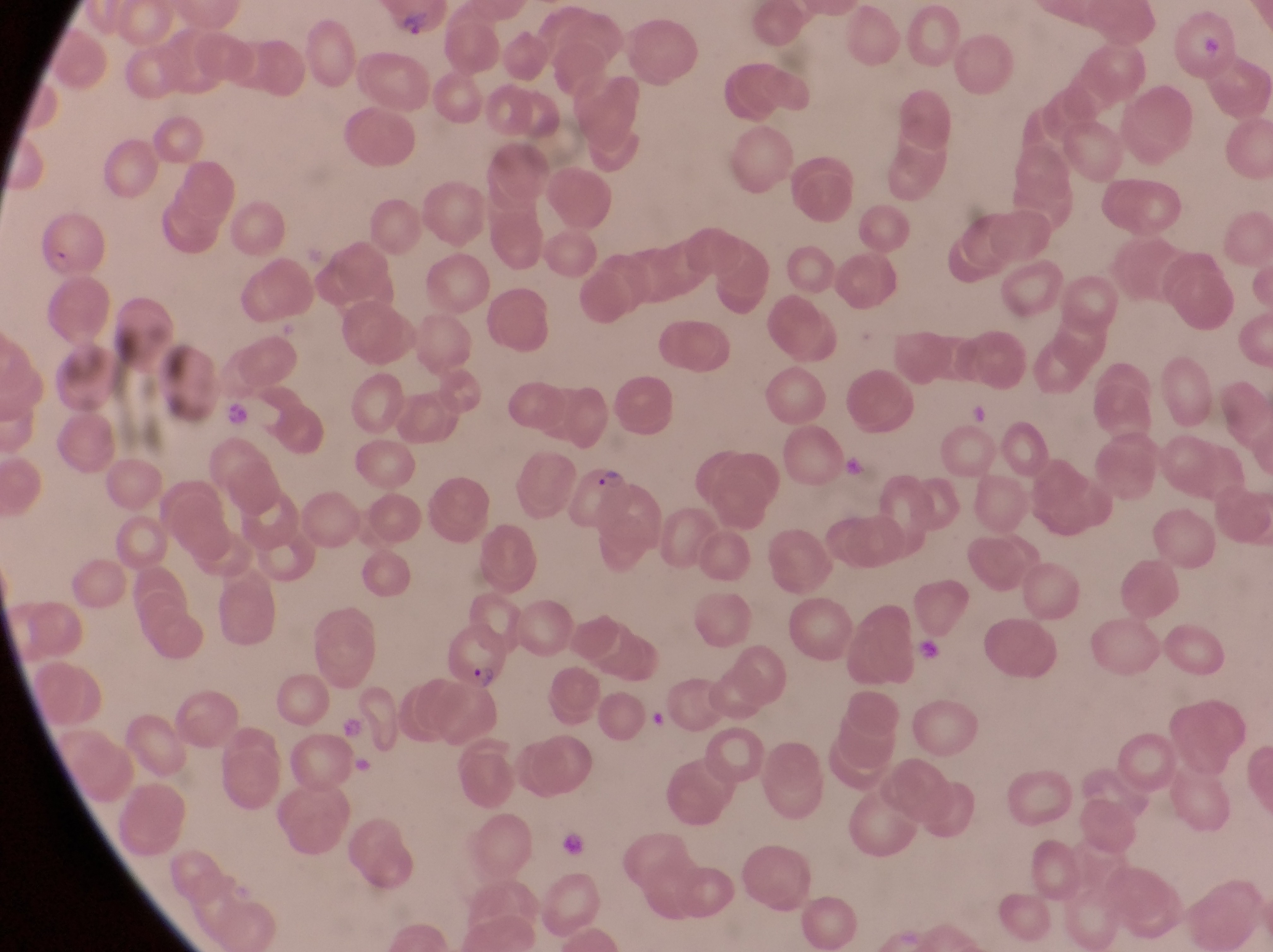

Approximate bounding boxes as {left, top, right, bottom} in pixels.
Summary:
  - Parasitised red blood cell locations: {25, 202, 108, 284}, {567, 465, 629, 530}, {444, 629, 518, 696}
  - Trophozoite locations: {221, 401, 255, 430}
  - Artifact (platelet-like body, stain precipitate, or debris) locations: {847, 451, 868, 479}, {922, 642, 946, 668}, {337, 716, 368, 743}, {561, 833, 587, 859}
  - Capture: smartphone photograph through the eyepiece of an Olympus CX-23 microscope
  - Magnification: 1000x
  - Country: Uganda
  - Preparation: thin blood smear
  - Field of view: single
  - Image size: 1273×952 pixels